Report the malaria status.
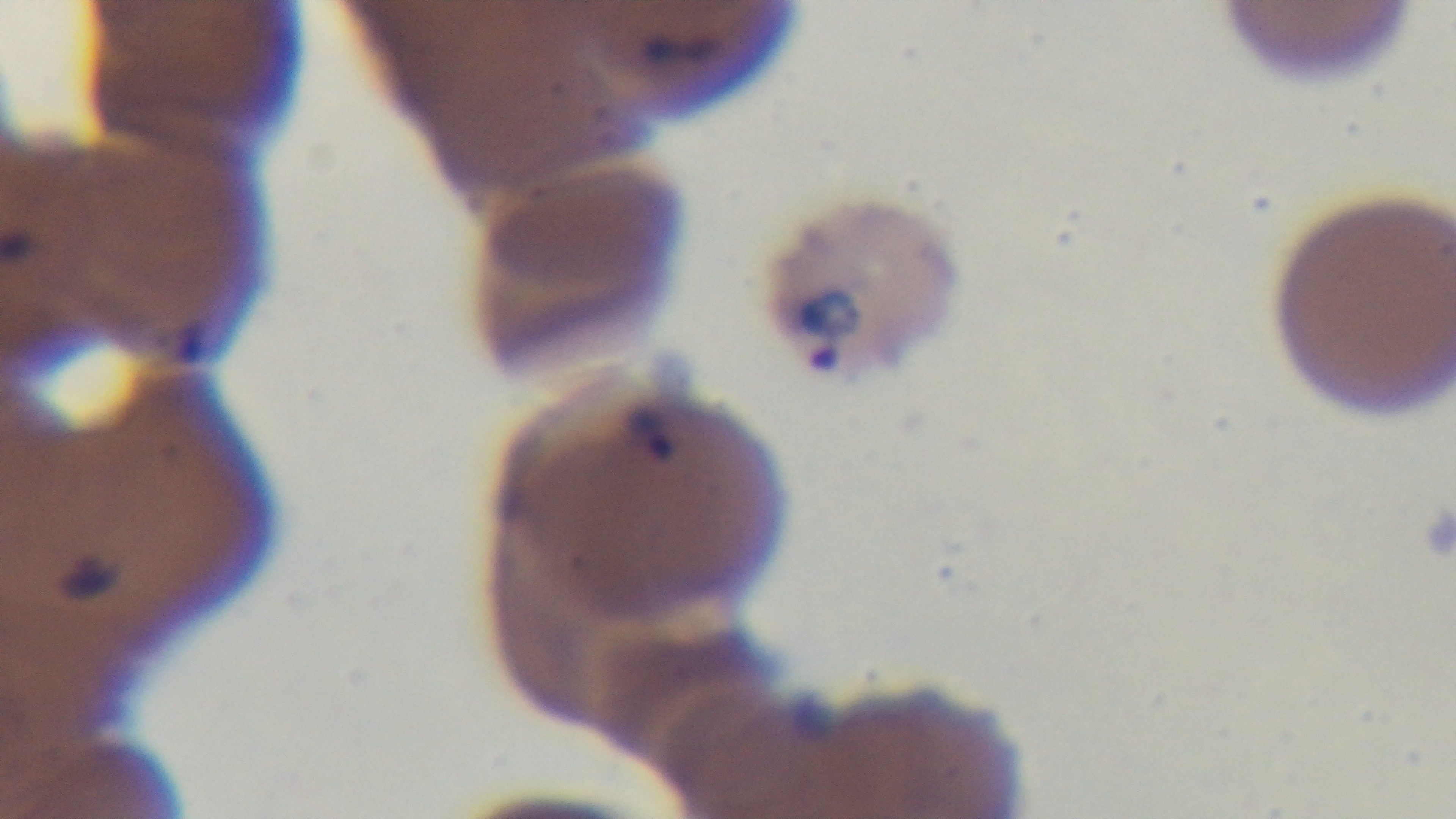
It is infected.

{
  "stain": "Giemsa",
  "capture": "mounted 4K digital camera",
  "objective": "100x oil immersion",
  "modality": "light microscopy",
  "preparation": "thin",
  "field_of_view": "one from the slide"
}